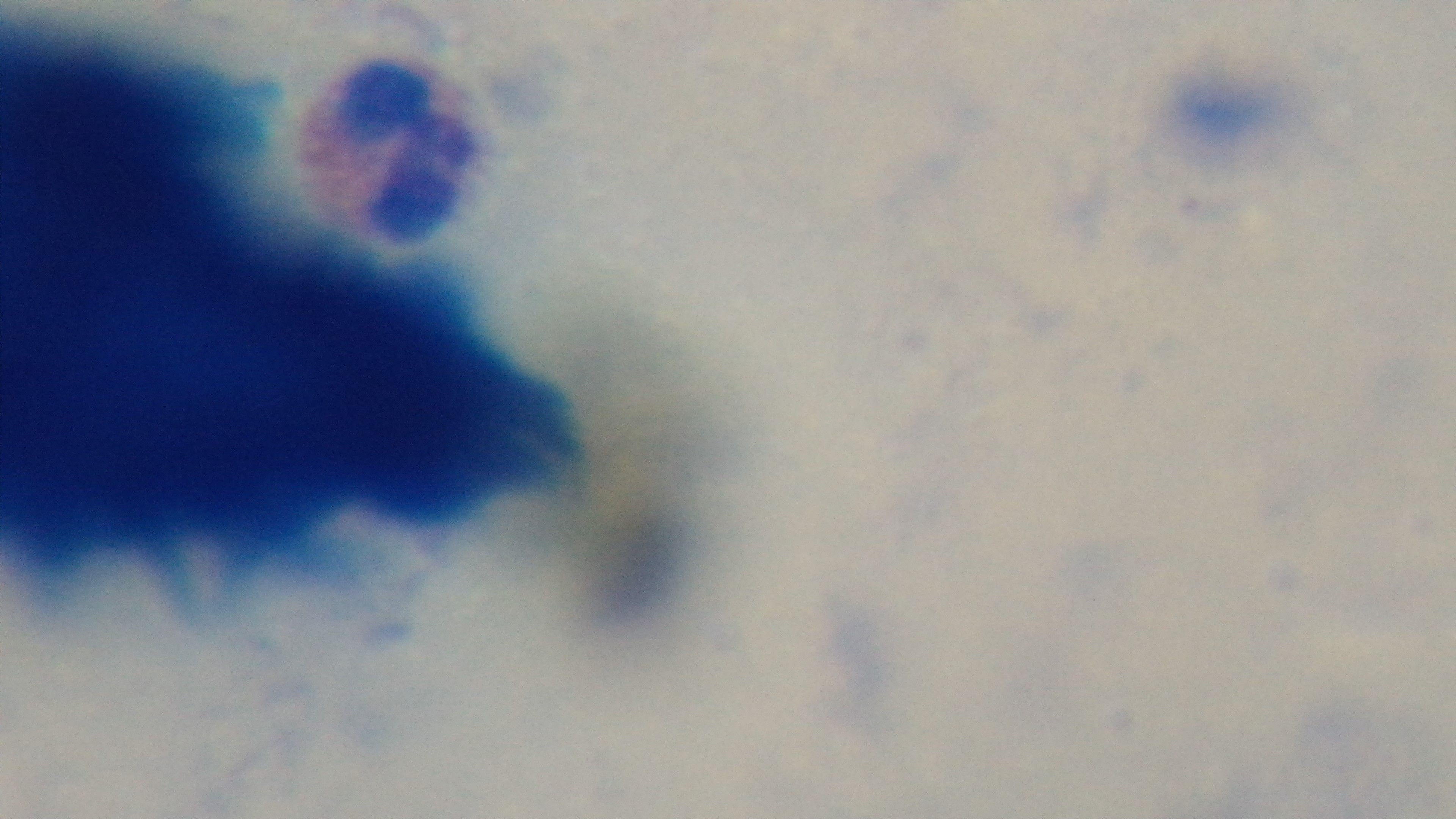
100x oil-immersion objective. Preparation: thick blood film. Single field of view. Photomicrograph. Malaria status: negative. Mounted 4K digital camera. Giemsa stain.